Classify this cell by malaria status.
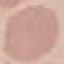

Uninfected.

preparation = thin smear
stain = Giemsa
capture = smartphone camera at the microscope eyepiece
image type = automatically extracted cell patch, resized to 64 × 64 pixels